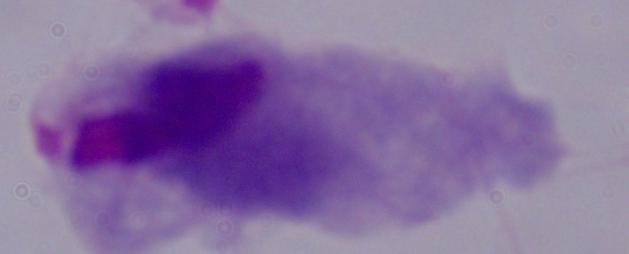 1000x magnification. Micrograph. A trichomonad is seen.